State which parasite is depicted.
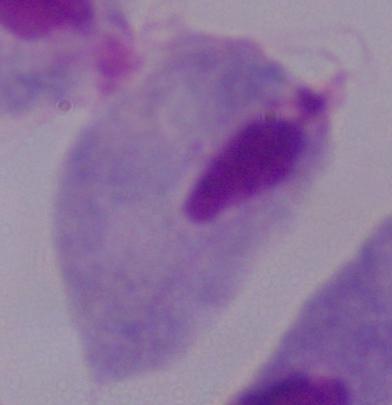
This is a trichomonad.

Photomicrograph. Captured at 1000x magnification.